Assess this cell for malaria.
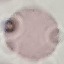
It is uninfected.

Photographed with a smartphone camera at the microscope eyepiece. Thin blood film. Giemsa stain. Automatically extracted cell patch, resized to 64 × 64 pixels.